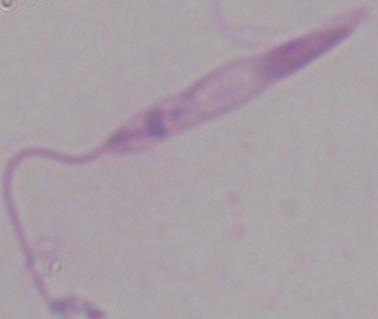 A Leishmania parasite is shown. Captured at 1000x magnification. Photomicrograph.